Name the parasite shown.
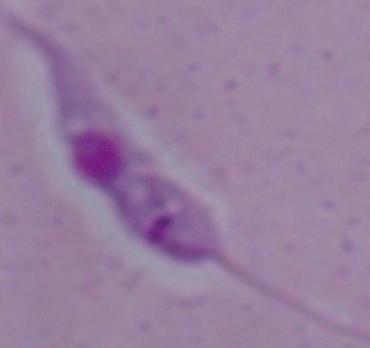

Leishmania.

Photomicrograph. 1000x magnification.